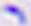

{
  "modality": "photomicrograph",
  "identification": "Toxoplasma gondii",
  "magnification": "400x"
}